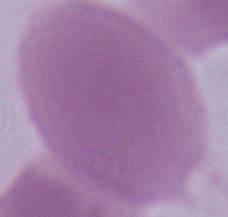
Summary:
  - Magnification: 1000x
  - Identification: red blood cell
  - Modality: micrograph